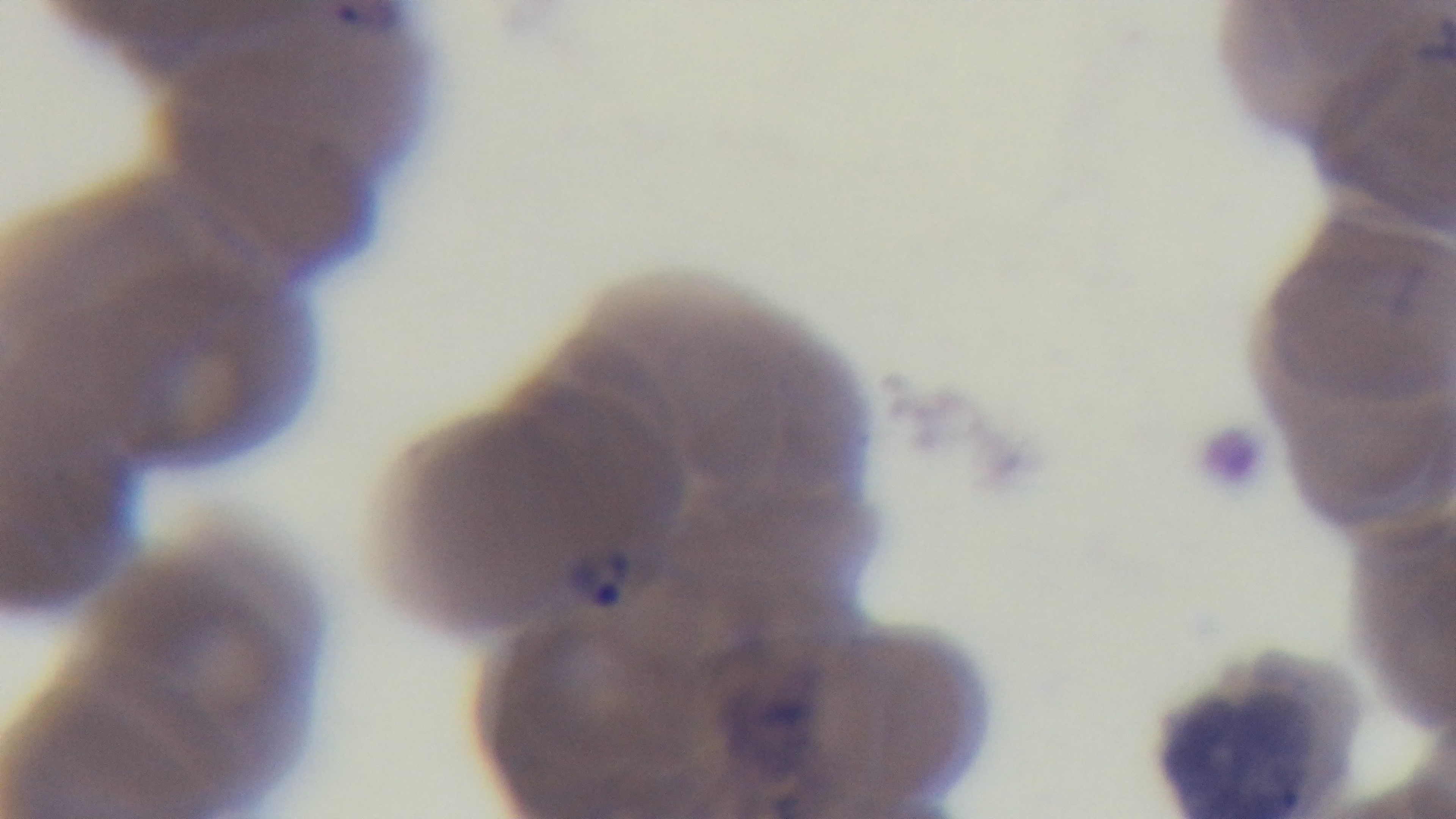

preparation: thin
capture: mounted 4K digital camera
objective: 100x oil immersion
stain: Giemsa
modality: light microscopy
field_of_view: one from the slide
malaria_status: positive